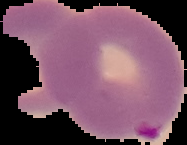
image size = 187×145 pixels
image type = segmented cell region on a black background
malaria status = parasitized
preparation = thin blood film